Locate every blood parasite and identify its species.
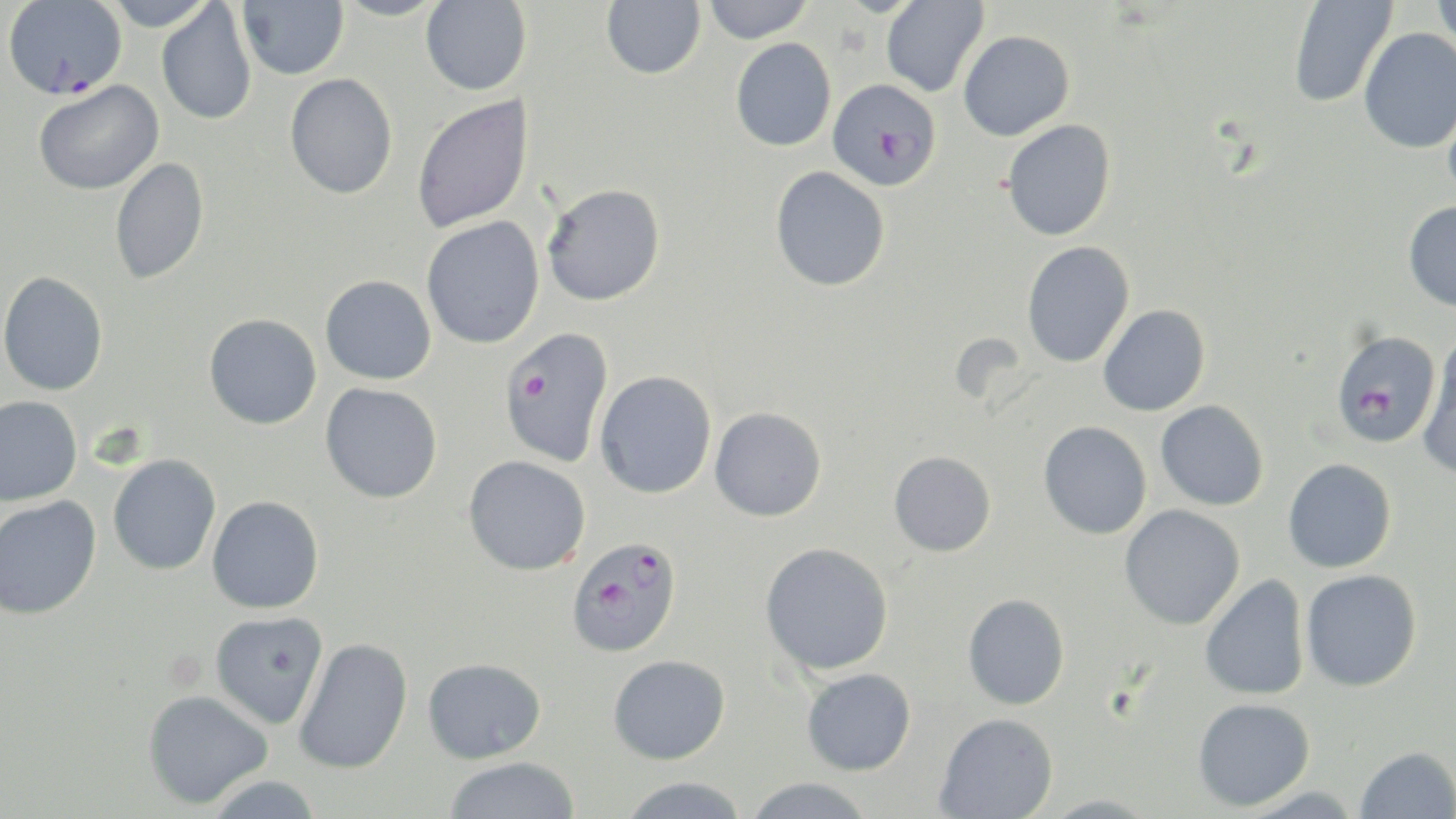

Approximate bounding boxes as named x1/y1/x2/y2 corners in pixels.
Plasmodium falciparum-infected red blood cells: (x1=3, y1=1, x2=127, y2=99), (x1=827, y1=78, x2=942, y2=190), (x1=499, y1=328, x2=614, y2=468), (x1=1330, y1=328, x2=1442, y2=449), (x1=566, y1=536, x2=682, y2=658).
No Plasmodium ovale, Plasmodium malariae, Plasmodium vivax, Babesia divergens, or Trypanosoma brucei observed.

Uninfected red blood cell locations: (x1=102, y1=0, x2=217, y2=31), (x1=237, y1=0, x2=349, y2=80), (x1=330, y1=0, x2=451, y2=21), (x1=421, y1=0, x2=532, y2=95), (x1=601, y1=0, x2=706, y2=79), (x1=701, y1=0, x2=816, y2=43), (x1=881, y1=0, x2=989, y2=98), (x1=1288, y1=0, x2=1397, y2=109), (x1=1431, y1=0, x2=1456, y2=60), (x1=156, y1=2, x2=257, y2=125), (x1=1358, y1=28, x2=1456, y2=153), (x1=958, y1=30, x2=1074, y2=141), (x1=730, y1=37, x2=837, y2=152), (x1=284, y1=73, x2=398, y2=199), (x1=33, y1=80, x2=163, y2=195), (x1=411, y1=94, x2=535, y2=234), (x1=1443, y1=95, x2=1456, y2=206), (x1=1001, y1=119, x2=1116, y2=241), (x1=110, y1=157, x2=210, y2=286), (x1=770, y1=166, x2=890, y2=292), (x1=542, y1=183, x2=666, y2=306), (x1=1402, y1=201, x2=1456, y2=312), (x1=421, y1=216, x2=545, y2=349), (x1=1021, y1=241, x2=1135, y2=369), (x1=0, y1=271, x2=108, y2=396), (x1=320, y1=274, x2=436, y2=385), (x1=1098, y1=304, x2=1210, y2=416), (x1=203, y1=313, x2=322, y2=430), (x1=1417, y1=335, x2=1456, y2=481), (x1=594, y1=370, x2=717, y2=499), (x1=320, y1=382, x2=443, y2=504), (x1=0, y1=395, x2=83, y2=507), (x1=1155, y1=400, x2=1269, y2=511), (x1=710, y1=406, x2=827, y2=521), (x1=1038, y1=421, x2=1152, y2=540), (x1=889, y1=451, x2=996, y2=557), (x1=108, y1=454, x2=221, y2=575), (x1=463, y1=456, x2=591, y2=576), (x1=1282, y1=458, x2=1396, y2=573), (x1=0, y1=495, x2=101, y2=620), (x1=207, y1=496, x2=324, y2=614), (x1=1119, y1=505, x2=1245, y2=630), (x1=759, y1=542, x2=894, y2=675), (x1=1301, y1=569, x2=1422, y2=692), (x1=1199, y1=573, x2=1310, y2=702), (x1=962, y1=593, x2=1070, y2=710), (x1=209, y1=611, x2=328, y2=729), (x1=293, y1=637, x2=413, y2=775), (x1=608, y1=655, x2=730, y2=765), (x1=422, y1=657, x2=546, y2=763), (x1=801, y1=668, x2=916, y2=776), (x1=143, y1=689, x2=273, y2=809), (x1=1192, y1=697, x2=1315, y2=811), (x1=935, y1=712, x2=1058, y2=818), (x1=1354, y1=745, x2=1456, y2=818), (x1=444, y1=756, x2=581, y2=818), (x1=204, y1=775, x2=324, y2=818), (x1=617, y1=777, x2=751, y2=818), (x1=741, y1=778, x2=878, y2=819), (x1=1037, y1=794, x2=1162, y2=817). Slide-level diagnosis: Plasmodium falciparum. Optical microscopy. 1000x magnification. Image is 1456×819 pixels. Single field of view. May-Grünwald-Giemsa-stained preparation. Thin blood film.